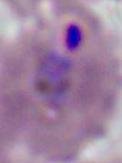

identification = Plasmodium
magnification = 400x or 1000x
modality = micrograph